Point out each leukocyte.
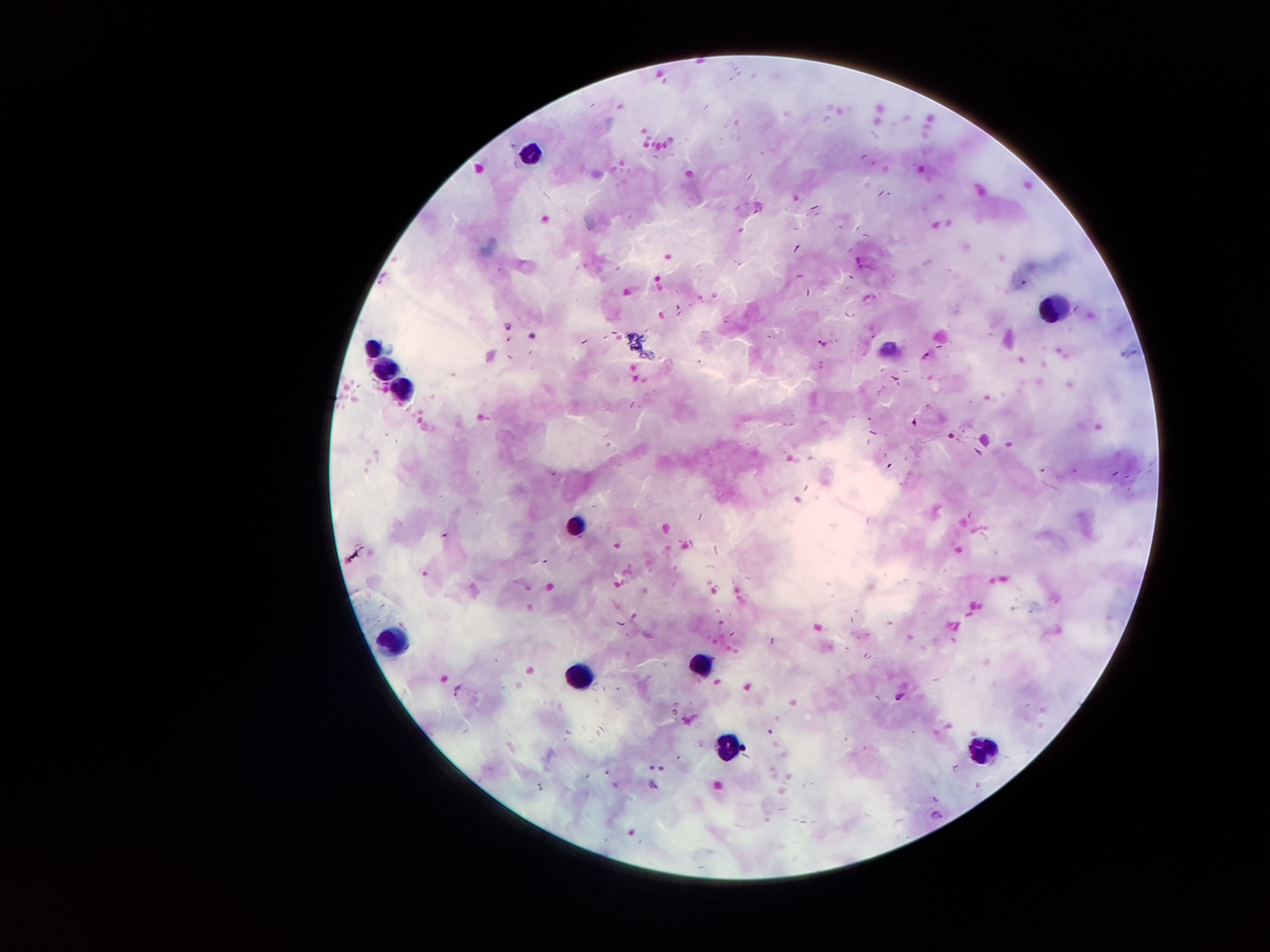

Approximate object centers, in pixels from the top-left corner.
Leukocytes: (x=531, y=152), (x=1054, y=310), (x=373, y=349), (x=382, y=366), (x=405, y=395), (x=576, y=524), (x=395, y=640), (x=702, y=663), (x=576, y=681), (x=728, y=746), (x=980, y=749).

Plasmodium parasite locations: (x=820, y=343), (x=927, y=356), (x=456, y=691), (x=899, y=697), (x=938, y=814). Smartphone photograph taken through the microscope eyepiece. Thick peripheral-blood smear. Patient malaria status: infected with Plasmodium falciparum. One field from this slide. Image is 1270×952 pixels. Giemsa stain. 100x magnification.